State which parasite is depicted.
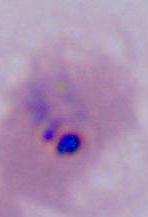

Plasmodium.

Summary:
  - Modality: micrograph
  - Magnification: 400x or 1000x